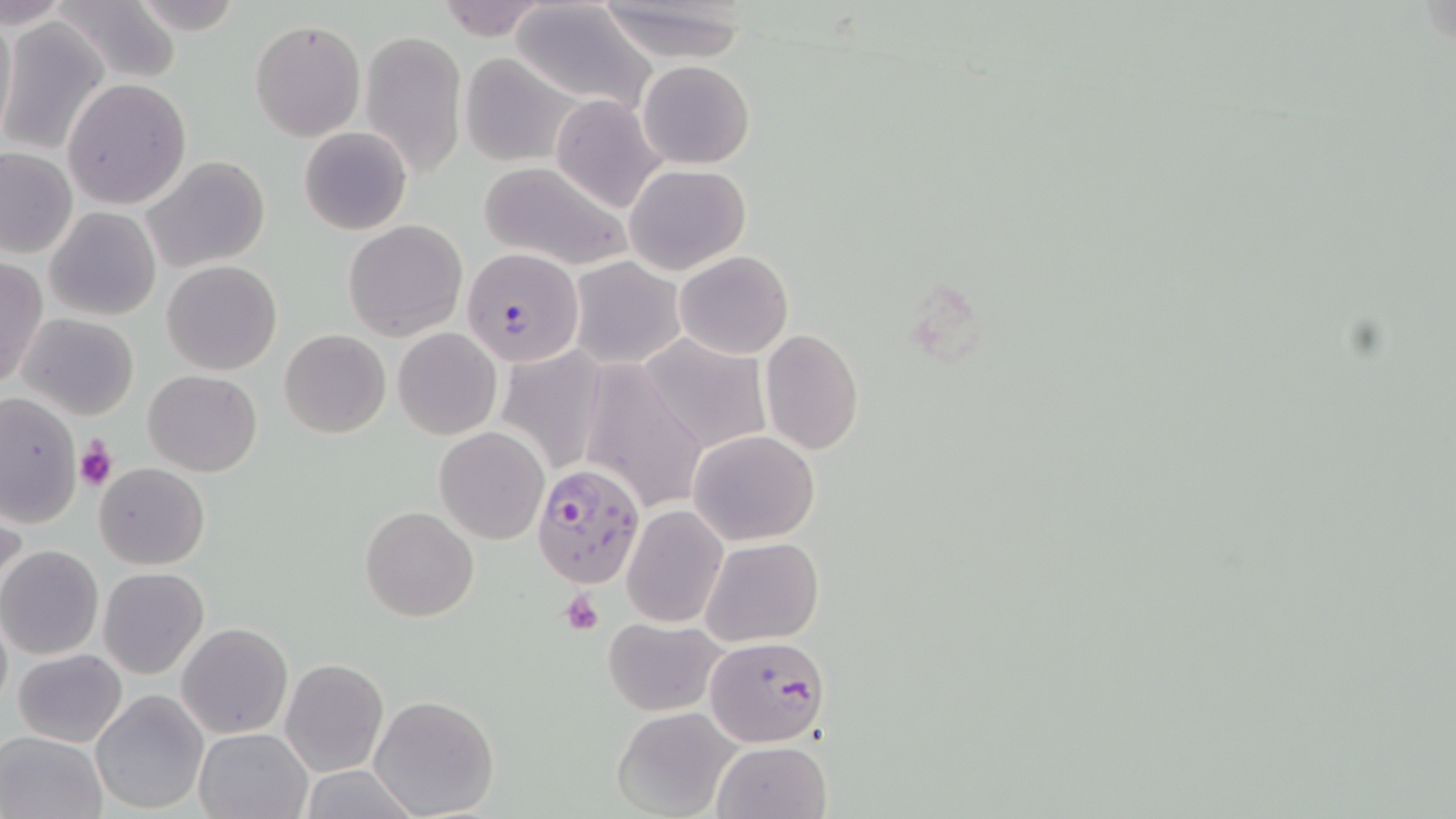

Approximate bounding boxes as [x1, y1, x2, y2] in pixels. Plasmodium falciparum-infected red blood cell locations: [463, 247, 584, 368], [532, 462, 646, 588], [704, 634, 831, 746]. Uninfected red blood cell locations: [52, 0, 184, 86], [432, 0, 552, 41], [588, 0, 762, 62], [0, 1, 70, 32], [509, 2, 658, 114], [0, 4, 17, 144], [0, 18, 110, 156], [249, 19, 365, 141], [358, 28, 468, 179], [457, 53, 584, 166], [638, 59, 755, 168], [62, 78, 194, 210], [551, 94, 668, 213], [298, 126, 411, 235], [1, 148, 76, 258], [143, 156, 271, 272], [479, 162, 632, 272], [624, 164, 750, 275], [46, 207, 161, 320], [344, 219, 468, 341], [674, 249, 794, 359], [567, 256, 684, 370], [0, 257, 47, 391], [161, 260, 282, 376], [19, 313, 140, 420], [393, 327, 501, 439], [280, 329, 390, 438], [759, 329, 863, 457], [637, 333, 770, 454], [495, 346, 607, 476], [578, 365, 707, 516], [142, 369, 264, 476], [1, 393, 81, 527], [435, 427, 549, 544], [687, 429, 822, 545], [94, 463, 210, 569], [622, 504, 730, 627], [360, 505, 479, 622], [2, 509, 27, 615], [699, 536, 823, 645], [0, 545, 104, 660], [98, 566, 209, 678], [602, 617, 728, 715], [177, 622, 293, 739], [11, 649, 128, 746], [281, 657, 388, 778], [90, 690, 210, 815], [368, 695, 500, 818], [612, 705, 741, 818], [194, 729, 311, 818], [0, 730, 107, 818], [711, 740, 833, 819]. Platelet locations: [74, 438, 117, 492], [560, 589, 604, 634]. Slide-level diagnosis: Plasmodium falciparum. Single field of view. 1000x magnification. Thin blood smear. Image is 1456×819 pixels. May-Grünwald-Giemsa-stained preparation. Light microscopy.